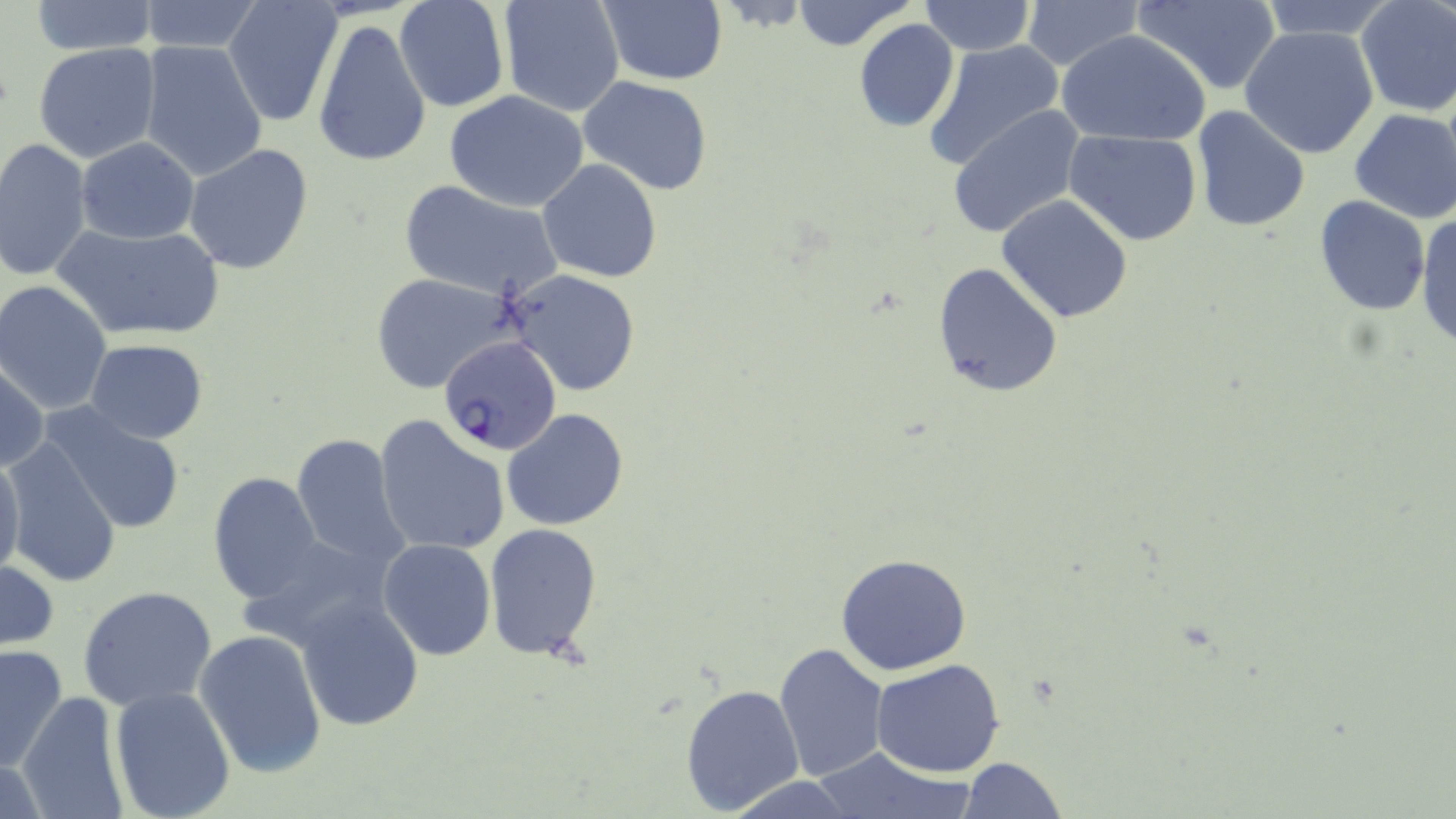

Summary:
  - Coordinate format: approximate bounding boxes as [x1, y1, x2, y2] in pixels
  - Plasmodium falciparum-infected red blood cell locations: [438, 338, 563, 454]
  - Uninfected red blood cell locations: [28, 0, 162, 55], [135, 0, 266, 54], [223, 0, 343, 125], [394, 0, 509, 112], [498, 0, 626, 117], [600, 0, 729, 85], [789, 0, 919, 52], [1020, 0, 1142, 74], [1132, 0, 1282, 94], [1256, 0, 1396, 40], [919, 1, 1036, 55], [1354, 1, 1456, 117], [852, 18, 959, 131], [313, 20, 431, 168], [1240, 26, 1381, 159], [1059, 29, 1213, 146], [138, 39, 270, 183], [921, 39, 1067, 174], [33, 43, 162, 164], [578, 76, 714, 195], [444, 89, 592, 211], [946, 105, 1086, 239], [1191, 107, 1310, 230], [1348, 108, 1456, 224], [1067, 129, 1203, 245], [76, 138, 199, 243], [1, 139, 92, 284], [183, 143, 315, 273], [537, 158, 664, 283], [397, 179, 562, 301], [996, 194, 1135, 324], [1312, 196, 1431, 316], [1415, 210, 1456, 350], [50, 222, 226, 343], [933, 262, 1063, 399], [501, 268, 643, 396], [369, 271, 520, 395], [1, 281, 115, 415], [84, 338, 209, 444], [1, 358, 48, 473], [42, 404, 188, 535], [502, 408, 631, 531], [372, 414, 514, 556], [288, 435, 410, 572], [3, 440, 121, 587], [0, 448, 25, 582], [207, 472, 324, 605], [482, 522, 603, 664], [377, 538, 495, 660], [834, 554, 973, 675], [0, 557, 61, 651], [77, 585, 217, 711], [295, 592, 424, 731], [193, 629, 328, 779], [774, 642, 889, 781], [0, 643, 69, 775], [872, 658, 1005, 777], [680, 682, 804, 815], [109, 684, 237, 818], [14, 691, 129, 818], [810, 746, 973, 818], [959, 757, 1069, 818], [723, 776, 856, 817]
  - Slide-level diagnosis: Plasmodium falciparum
  - Modality: optical microscopy
  - Magnification: 1000x
  - Stain: May-Grünwald-Giemsa
  - Preparation: thin blood film
  - Image size: 1456×819 pixels
  - Field of view: single